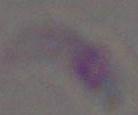

Summary:
  - Identification: Toxoplasma gondii
  - Modality: micrograph
  - Magnification: 1000x